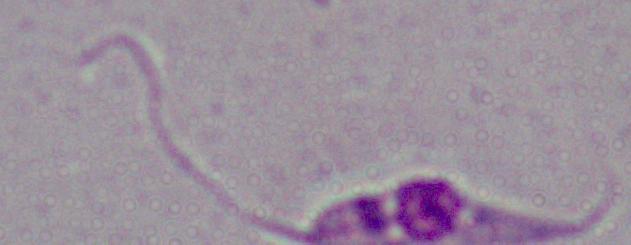
Summary:
  - Identification: Leishmania
  - Modality: photomicrograph
  - Magnification: 1000x